Describe the morphology of the erythrocytes.
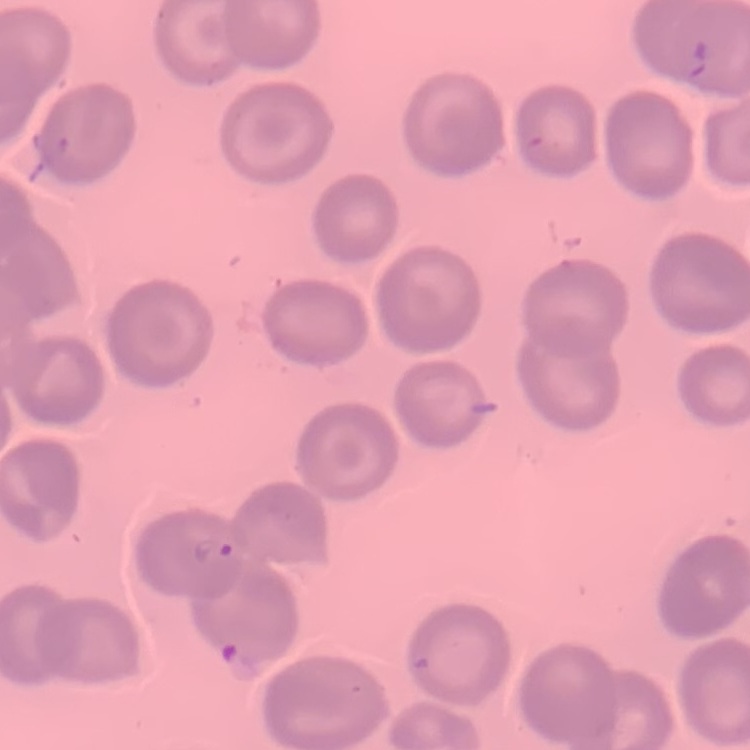

They show no rouleaux formation.

Thin blood smear. Field's or Giemsa stain. Square crop of a larger photomicrograph.